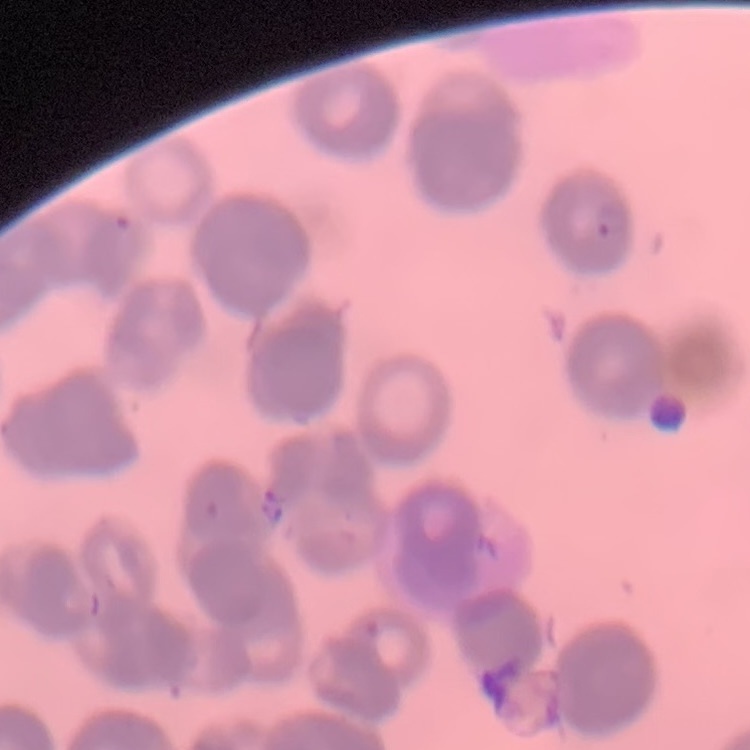
{
  "erythrocyte_morphology": "rouleaux formation",
  "stain": "Field's or Giemsa",
  "image_type": "square crop of a larger photomicrograph",
  "preparation": "thin blood film"
}